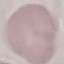 Malaria status: uninfected. Acquired by smartphone through the microscope eyepiece. Cell patch, automatically extracted from a larger field of view and resized to 64 × 64 pixels. Thin blood smear. Giemsa-stained preparation.